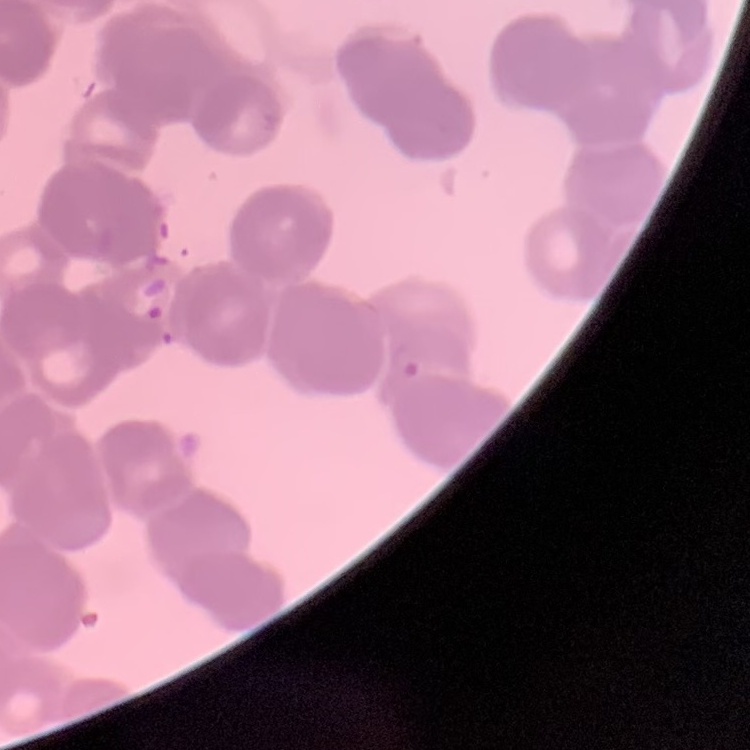

The erythrocytes show rouleaux formation. Field's or Giemsa stain. Thin peripheral smear. Square crop of a larger photomicrograph.